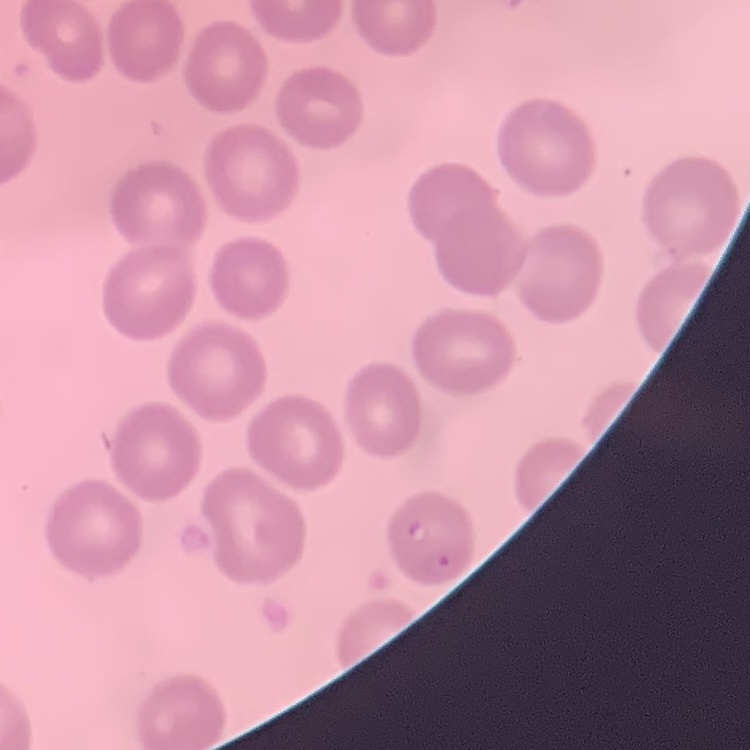
erythrocyte morphology = no rouleaux formation
preparation = thin blood smear
image type = square crop of a larger photomicrograph
stain = Field's or Giemsa